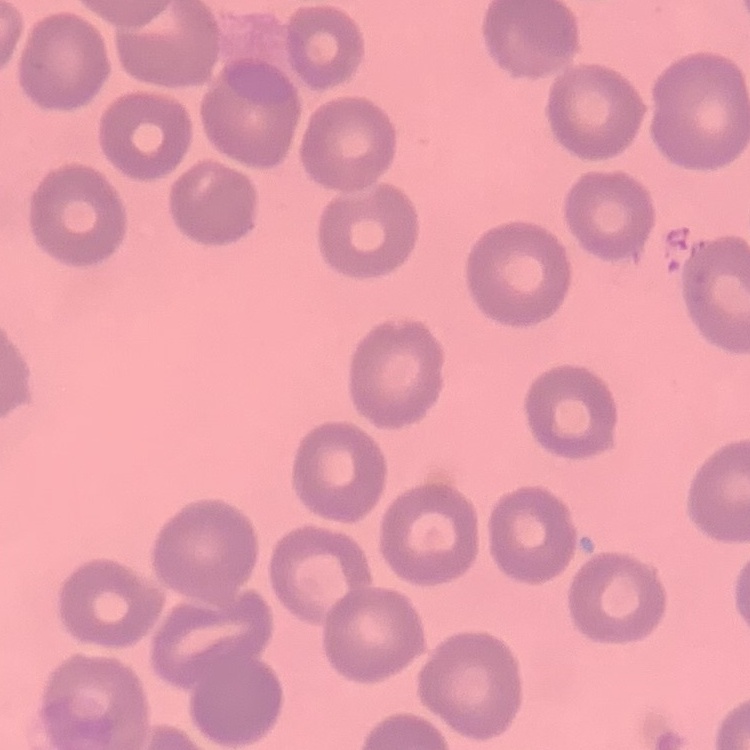
Summary:
  - Red blood cell morphology: no rouleaux formation
  - Stain: Field's or Giemsa
  - Preparation: thin blood smear
  - Image type: one tile cut from a larger photomicrograph